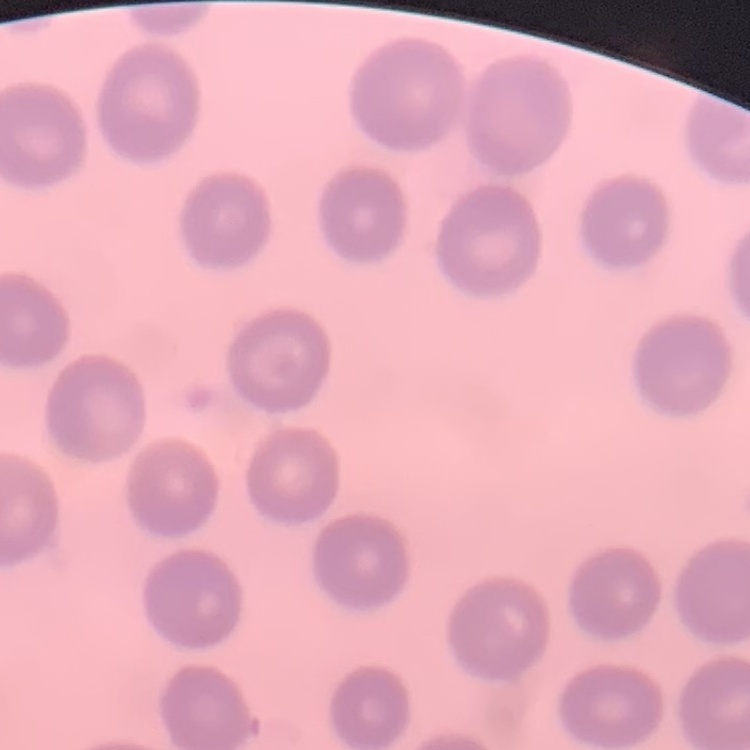

Summary:
  - Red blood cell morphology: no rouleaux formation
  - Stain: Field's or Giemsa
  - Image type: one tile cut from a larger photomicrograph
  - Preparation: thin peripheral smear